Assess this cell for malaria.
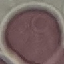
It is uninfected.

Thin blood smear. Cell patch, automatically extracted from a larger field of view and resized to 64 × 64 pixels. Acquired by smartphone through the microscope eyepiece. Giemsa-stained preparation.